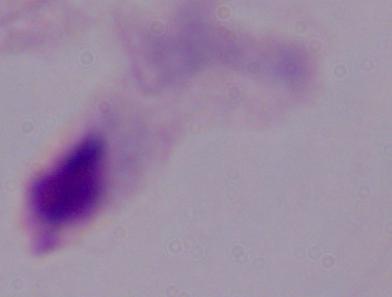

magnification = 1000x
modality = micrograph
identification = trichomonad